Mark where leukocytes are.
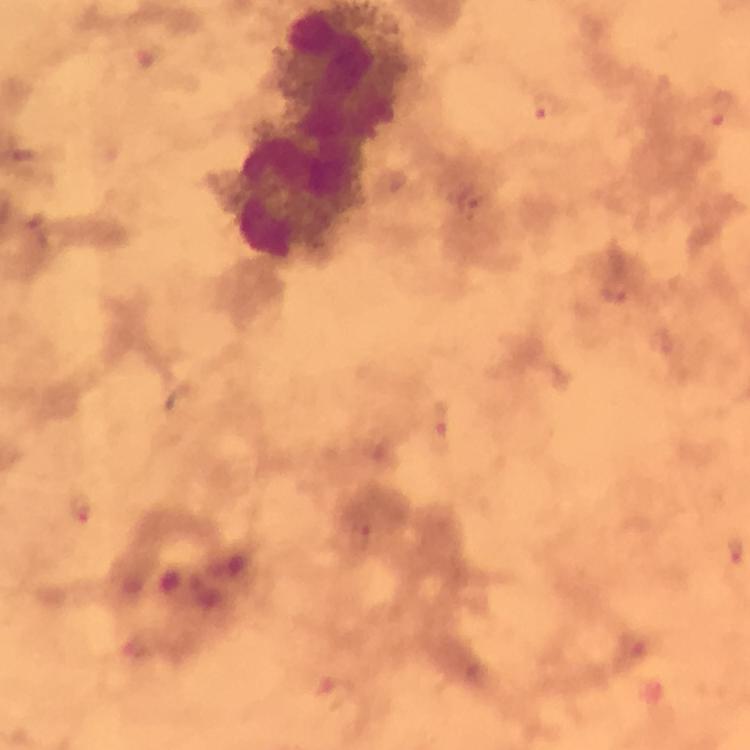
Approximate object centers, in pixels from the top-left corner.
Leukocytes: (x=299, y=201).

Plasmodium parasite locations: (x=545, y=106), (x=720, y=108), (x=24, y=154), (x=472, y=200), (x=38, y=228), (x=616, y=287), (x=438, y=421), (x=82, y=510), (x=359, y=537), (x=734, y=550), (x=334, y=693). At 100x magnification. Giemsa-stained preparation. Smartphone photograph taken through a microscope. Immersion oil was used. A crop from one field of view. Image is 750×750 pixels. From a malaria diagnostic workup. Thick blood film.